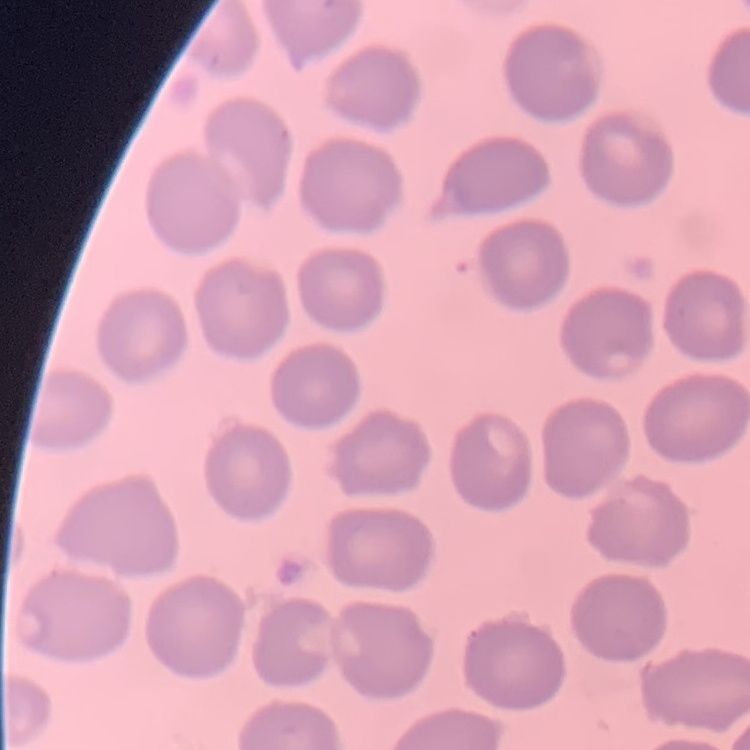

The erythrocytes exhibit no rouleaux formation. Square crop of a larger photomicrograph. Thin blood film. Stained with either Field's or Giemsa.